Describe the morphology of the erythrocytes.
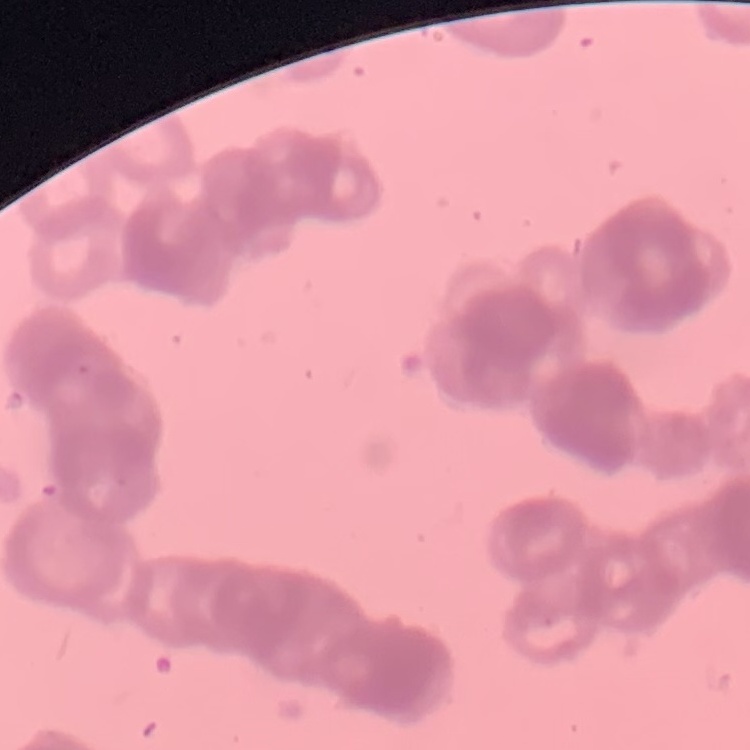
They show rouleaux formation.

preparation = thin blood film
image type = one tile cut from a larger photomicrograph
stain = Field's or Giemsa